Outline each blood parasite and name the species.
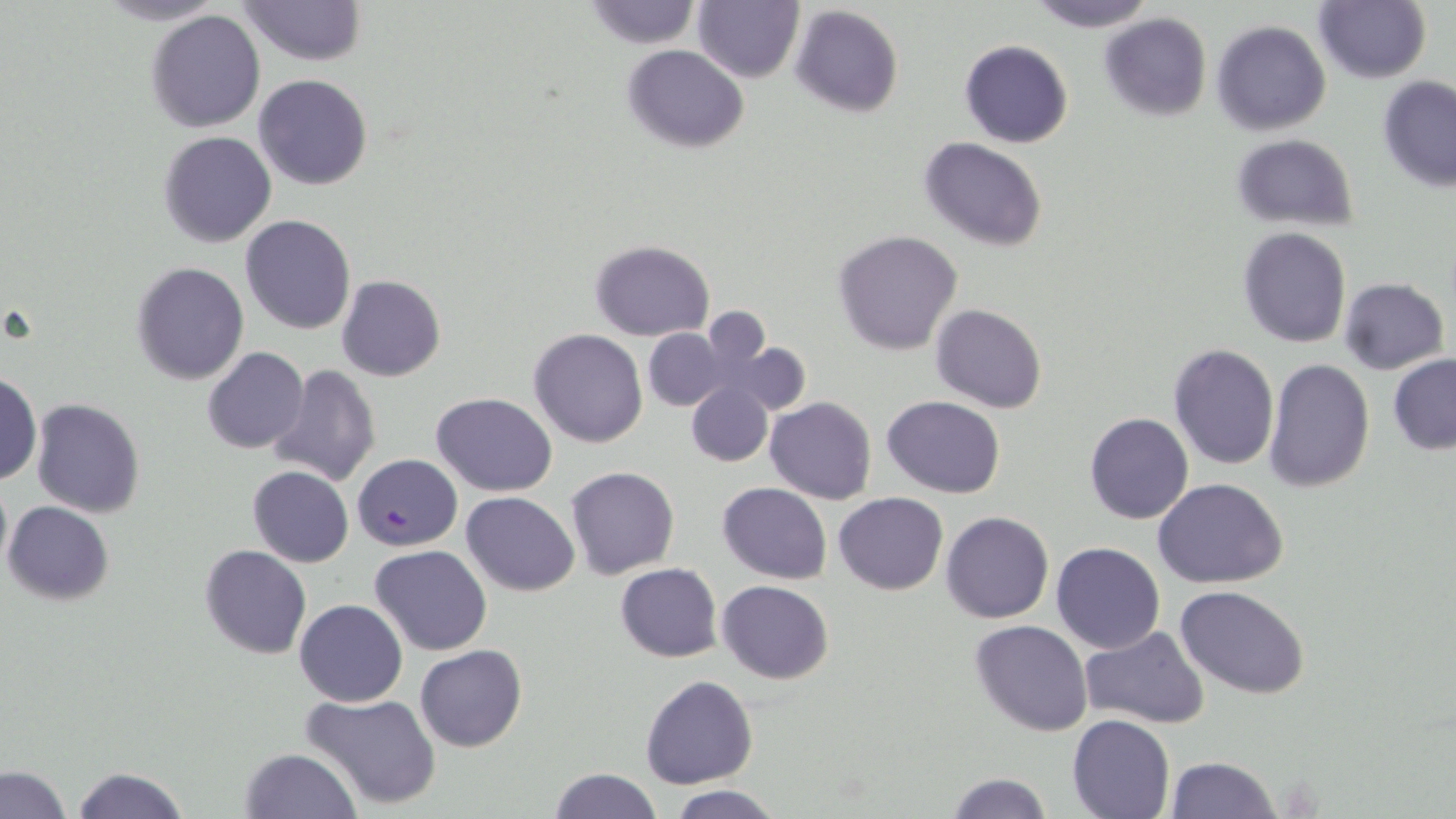

Approximate bounding boxes as (x1,y1)-(x2,y2) corner pairs in pixels.
Plasmodium falciparum-infected red blood cells: (352,452)-(461,551).
No Plasmodium ovale, Plasmodium malariae, Plasmodium vivax, Babesia divergens, or Trypanosoma brucei observed.

Summary:
  - Uninfected red blood cell locations: (92,0)-(230,26), (238,0)-(366,66), (693,0)-(804,83), (1029,0)-(1157,32), (1315,0)-(1430,84), (582,1)-(702,49), (789,4)-(904,117), (144,8)-(267,133), (1100,13)-(1212,121), (1210,20)-(1330,136), (959,40)-(1072,148), (622,44)-(750,151), (253,74)-(373,191), (1378,75)-(1456,191), (158,130)-(276,247), (1230,133)-(1358,230), (918,136)-(1047,251), (240,215)-(356,334), (1238,226)-(1353,348), (833,230)-(963,355), (588,240)-(714,340), (131,263)-(249,384), (337,274)-(445,381), (1340,278)-(1448,373), (931,304)-(1047,414), (642,328)-(729,411), (531,329)-(647,447), (713,338)-(812,416), (1168,344)-(1279,470), (203,346)-(309,454), (1388,354)-(1456,455), (1263,359)-(1375,493), (267,365)-(382,488), (1,372)-(41,485), (686,380)-(772,467), (432,391)-(556,495), (882,395)-(1006,497), (765,396)-(877,503), (30,398)-(145,518), (1084,413)-(1194,524), (248,465)-(353,567), (567,466)-(680,579), (0,470)-(12,580), (1155,477)-(1288,588), (717,482)-(832,583), (462,491)-(580,595), (834,491)-(948,594), (4,501)-(113,605), (941,511)-(1053,623), (1050,542)-(1165,653), (370,544)-(491,655), (200,545)-(310,659), (616,563)-(722,661), (718,580)-(834,684), (1177,585)-(1310,698), (294,599)-(408,707), (970,619)-(1092,736), (1081,625)-(1207,728), (415,644)-(526,751), (640,676)-(759,788), (301,692)-(441,811), (1067,714)-(1175,818), (239,747)-(362,818), (1166,756)-(1282,818), (2,765)-(71,818), (69,765)-(189,819), (547,767)-(661,819), (944,773)-(1052,818), (667,784)-(787,818)
  - Slide-level diagnosis: Plasmodium falciparum
  - Modality: light microscopy
  - Field of view: one of a larger specimen
  - Stain: May-Grünwald-Giemsa
  - Magnification: 1000x
  - Image size: 1456×819 pixels
  - Preparation: thin blood film